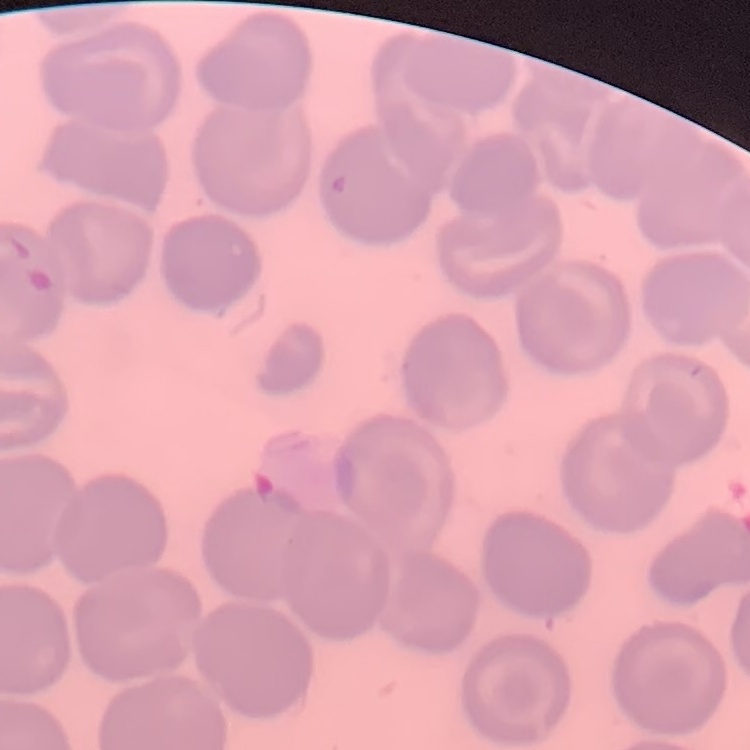

Summary:
  - Red blood cell morphology: no rouleaux formation
  - Image type: square crop of a larger photomicrograph
  - Preparation: thin blood film
  - Stain: Field's or Giemsa